Identify the blood parasite species.
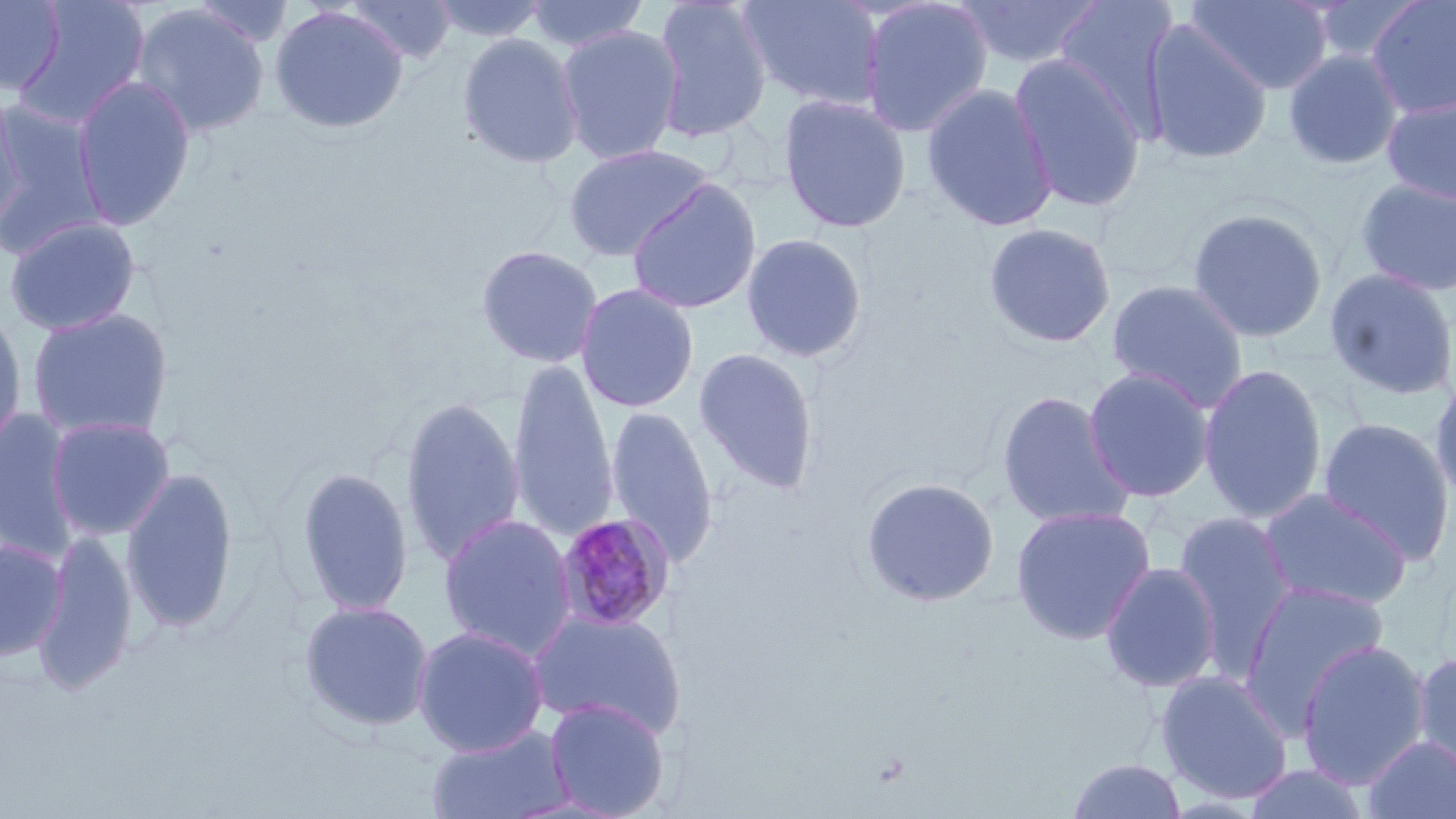
Plasmodium malariae.

Approximate bounding boxes as [x1, y1, x2, y2] in pixels. Plasmodium malariae-infected red blood cell locations: [554, 513, 676, 632]. Uninfected red blood cell locations: [12, 0, 151, 130], [346, 0, 458, 64], [427, 0, 551, 43], [526, 0, 651, 52], [650, 0, 773, 143], [737, 0, 884, 111], [858, 0, 995, 139], [955, 0, 1105, 70], [1053, 0, 1181, 139], [1187, 0, 1333, 95], [1364, 0, 1456, 118], [0, 1, 66, 95], [188, 1, 298, 49], [131, 4, 270, 138], [269, 5, 408, 134], [1141, 21, 1273, 165], [555, 25, 685, 165], [457, 32, 584, 169], [1283, 48, 1404, 170], [1008, 53, 1148, 212], [71, 76, 196, 231], [921, 82, 1058, 232], [777, 93, 912, 234], [0, 94, 28, 234], [1381, 94, 1456, 204], [0, 101, 106, 250], [563, 143, 718, 262], [626, 178, 762, 315], [1355, 178, 1456, 297], [1187, 207, 1328, 343], [3, 217, 141, 336], [983, 222, 1117, 349], [740, 232, 868, 364], [475, 244, 604, 368], [1323, 267, 1456, 402], [1106, 279, 1249, 411], [574, 283, 700, 413], [27, 308, 174, 440], [0, 309, 27, 455], [692, 347, 820, 496], [506, 360, 619, 544], [1198, 363, 1328, 524], [1082, 367, 1215, 503], [1428, 370, 1456, 507], [996, 391, 1135, 529], [400, 396, 525, 568], [605, 405, 719, 571], [0, 412, 81, 560], [1316, 416, 1455, 565], [46, 417, 175, 541], [296, 466, 413, 617], [121, 468, 239, 633], [860, 477, 1000, 607], [1258, 488, 1412, 612], [1010, 504, 1157, 645], [1172, 511, 1298, 678], [438, 514, 577, 660], [33, 532, 138, 694], [0, 538, 67, 660], [1099, 561, 1221, 693], [1239, 579, 1390, 735], [298, 600, 435, 732], [529, 609, 687, 740], [412, 625, 549, 757], [1296, 639, 1431, 788], [1411, 650, 1456, 782], [1155, 669, 1295, 805], [544, 698, 670, 818], [424, 725, 575, 818], [1362, 735, 1456, 819], [1065, 758, 1187, 818], [1241, 763, 1372, 819]. May-Grünwald-Giemsa stain. Optical microscopy. One field of a larger specimen. Thin blood smear. 1000x magnification. Image is 1456×819 pixels.